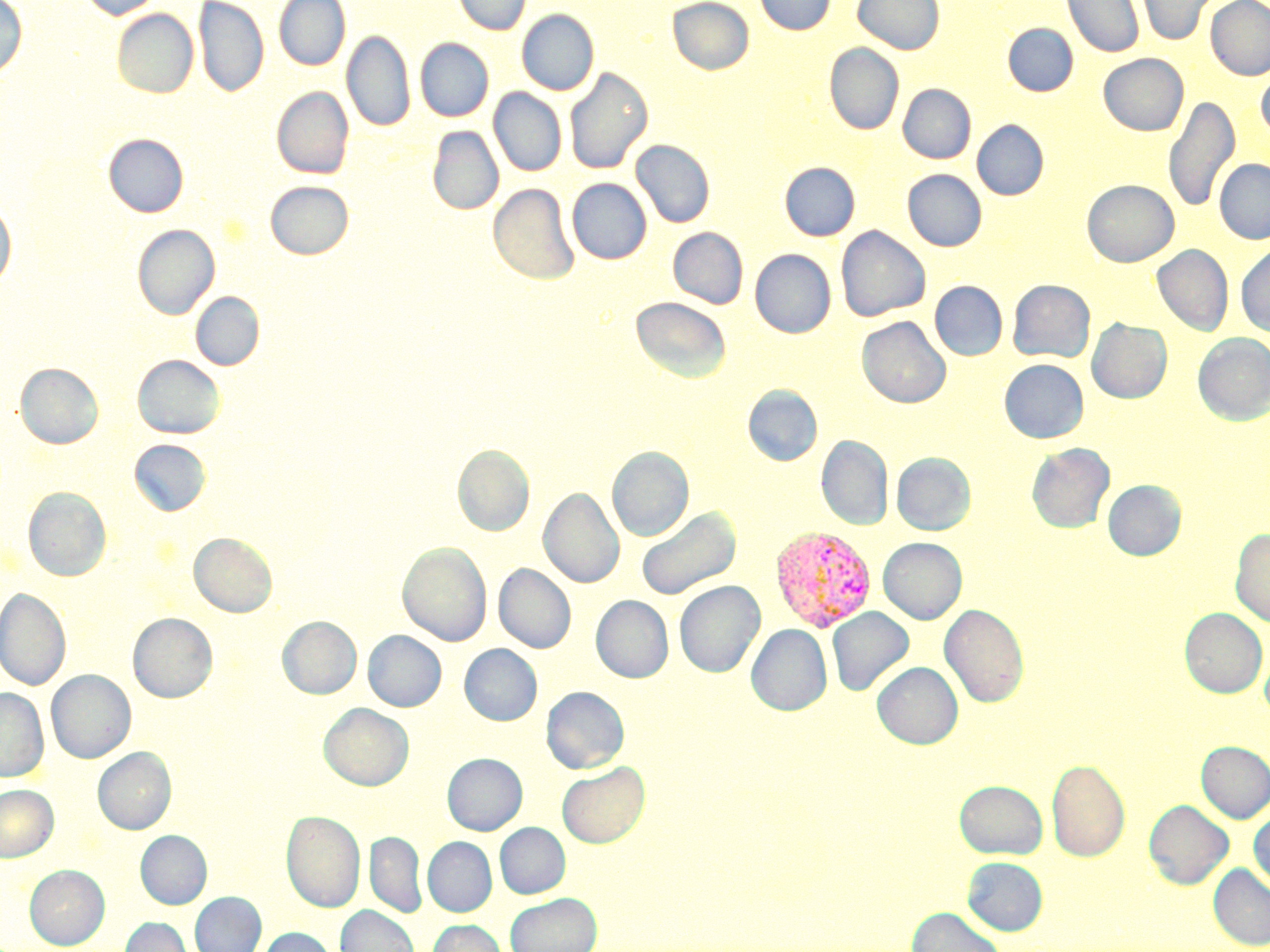

Approximate bounding boxes as (x1,y1)-(x2,y2) corner pairs in pixels. Plasmodium vivax-infected red blood cell locations: (769,526)-(876,632). Uninfected red blood cell locations: (0,0)-(27,78), (79,0)-(163,19), (193,0)-(268,98), (274,0)-(350,70), (453,0)-(531,35), (668,0)-(754,74), (755,0)-(835,35), (853,0)-(944,55), (1062,0)-(1144,58), (1206,0)-(1270,80), (1136,1)-(1215,46), (112,9)-(198,98), (517,9)-(598,95), (1003,23)-(1078,96), (342,29)-(414,133), (416,38)-(494,121), (825,43)-(904,134), (1099,53)-(1187,135), (1256,65)-(1270,141), (565,68)-(653,174), (898,84)-(976,163), (272,87)-(353,179), (489,88)-(566,176), (1163,96)-(1240,213), (972,120)-(1048,200), (428,126)-(503,215), (104,133)-(188,217), (631,140)-(715,228), (1215,158)-(1270,244), (780,162)-(859,241), (903,169)-(987,251), (567,178)-(651,264), (1082,179)-(1179,267), (266,181)-(353,259), (489,183)-(580,284), (0,203)-(16,289), (133,224)-(219,320), (836,225)-(930,322), (668,227)-(748,309), (1152,245)-(1233,336), (1236,245)-(1270,337), (751,249)-(835,337), (1008,279)-(1095,363), (930,281)-(1007,360), (190,292)-(264,371), (630,296)-(731,382), (857,316)-(951,408), (1087,318)-(1172,403), (1193,333)-(1270,425), (133,355)-(224,438), (1000,359)-(1088,443), (15,363)-(103,448), (743,385)-(822,465), (816,436)-(893,530), (129,439)-(210,516), (1027,443)-(1114,533), (452,445)-(534,535), (607,446)-(694,542), (892,453)-(976,535), (1103,480)-(1186,560), (23,487)-(111,581), (539,488)-(624,588), (636,507)-(740,601), (1231,528)-(1270,627), (189,533)-(277,616), (878,538)-(966,624), (398,542)-(491,646), (494,563)-(575,653), (675,580)-(765,677), (0,588)-(71,691), (591,595)-(673,683), (940,603)-(1029,708), (827,607)-(913,695), (1180,608)-(1268,698), (128,613)-(217,702), (278,616)-(361,698), (746,624)-(832,715), (364,630)-(446,711), (1260,642)-(1270,721), (460,644)-(542,725), (872,662)-(963,749), (46,670)-(135,763), (542,686)-(629,773), (0,688)-(48,782), (319,703)-(413,790), (1196,741)-(1270,822), (93,747)-(176,834), (443,753)-(527,835), (1047,759)-(1130,861), (557,762)-(650,848), (954,780)-(1047,858), (0,784)-(57,861), (1144,800)-(1233,889), (1249,807)-(1270,892), (282,810)-(364,911), (495,823)-(570,898), (136,831)-(211,909), (366,832)-(426,917), (423,837)-(496,916), (963,857)-(1048,935), (1208,864)-(1270,949), (25,865)-(109,949), (190,892)-(266,952), (506,893)-(601,952), (335,905)-(418,952), (906,906)-(1007,952), (121,917)-(192,952), (428,920)-(506,952), (260,927)-(336,952). Slide-level diagnosis: Plasmodium vivax. Image is 1270×952 pixels. 1000x magnification. Thin blood film. One field of a larger specimen. Optical microscopy. May-Grünwald-Giemsa-stained preparation.